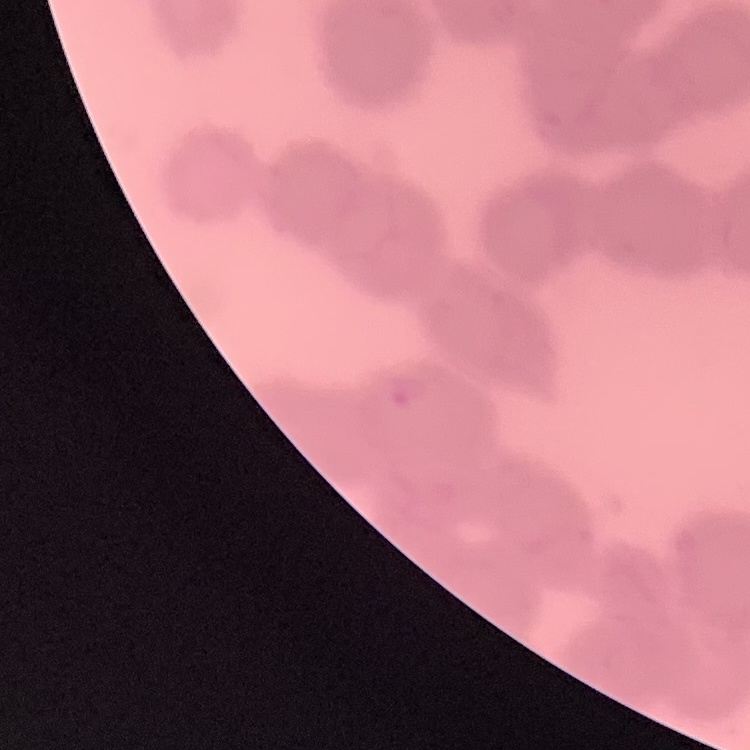
erythrocyte_morphology: rouleaux formation
stain: Field's or Giemsa
image_type: square crop of a larger photomicrograph
preparation: thin blood smear